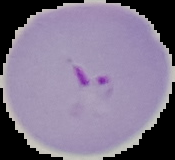

From a thin blood film. Result: Plasmodium parasites identified. Image is 175×160 pixels. Cell region segmented out of the field of view; the surrounding area is masked to black.